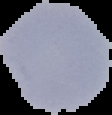

Summary:
  - Result: malaria parasites identified
  - Image size: 112×115 pixels
  - Image type: segmented cell region on a black background
  - Preparation: thin blood film